Outline every leukocyte.
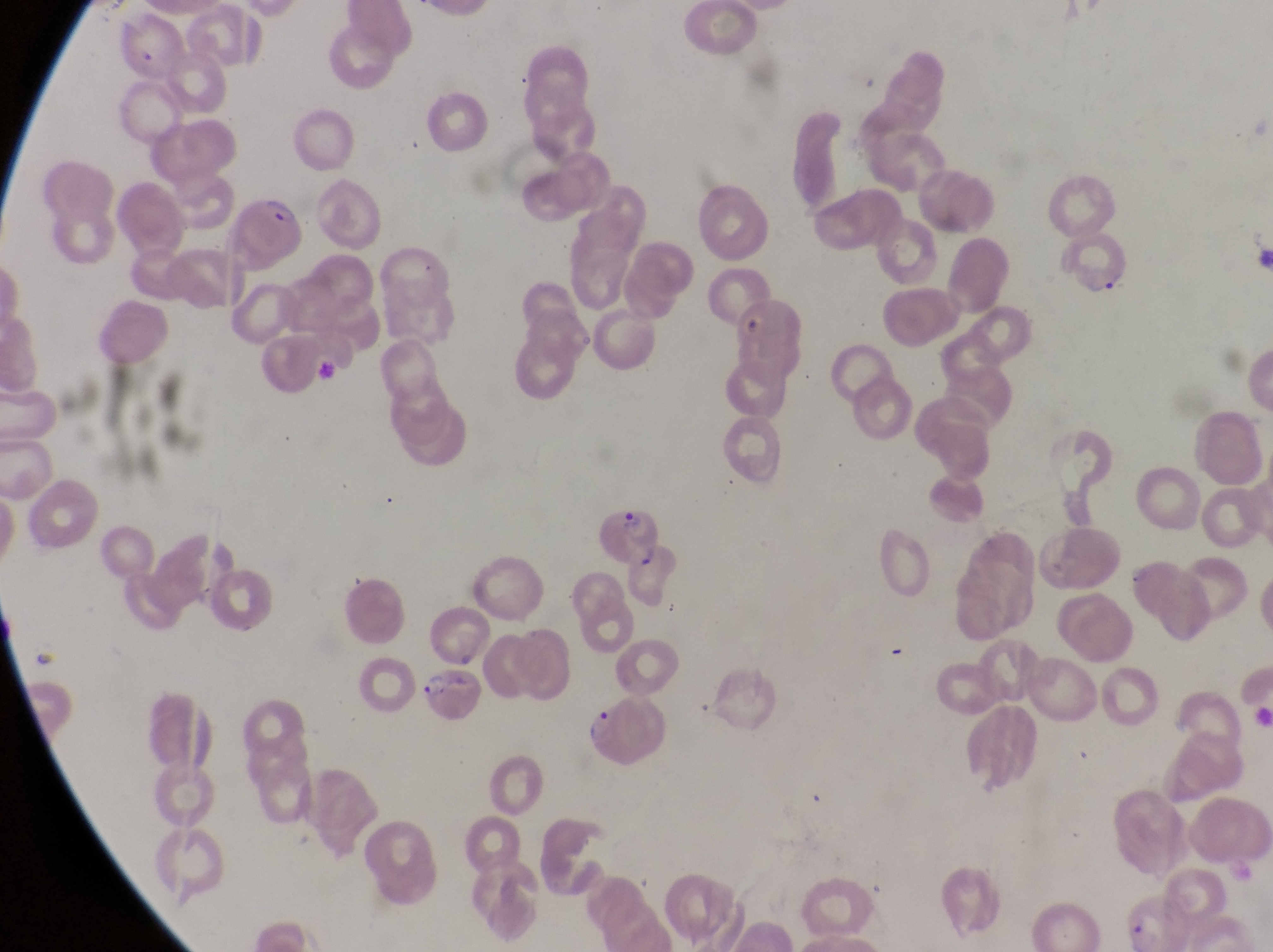

No leukocytes observed.

Approximate bounding boxes as {left, top, right, bottom} in pixels.
Summary:
  - Parasitised red blood cell locations: {220, 193, 312, 267}, {1066, 239, 1131, 304}, {597, 504, 660, 561}, {1123, 554, 1208, 649}, {414, 672, 484, 730}, {581, 696, 671, 781}
  - Preparation: thin blood smear
  - Capture: smartphone photograph through the eyepiece of an Olympus CX-23 microscope
  - Field of view: single
  - Image size: 1273×952 pixels
  - Country: Uganda
  - Magnification: 1000x